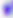

identification = Toxoplasma gondii
magnification = 400x
modality = photomicrograph